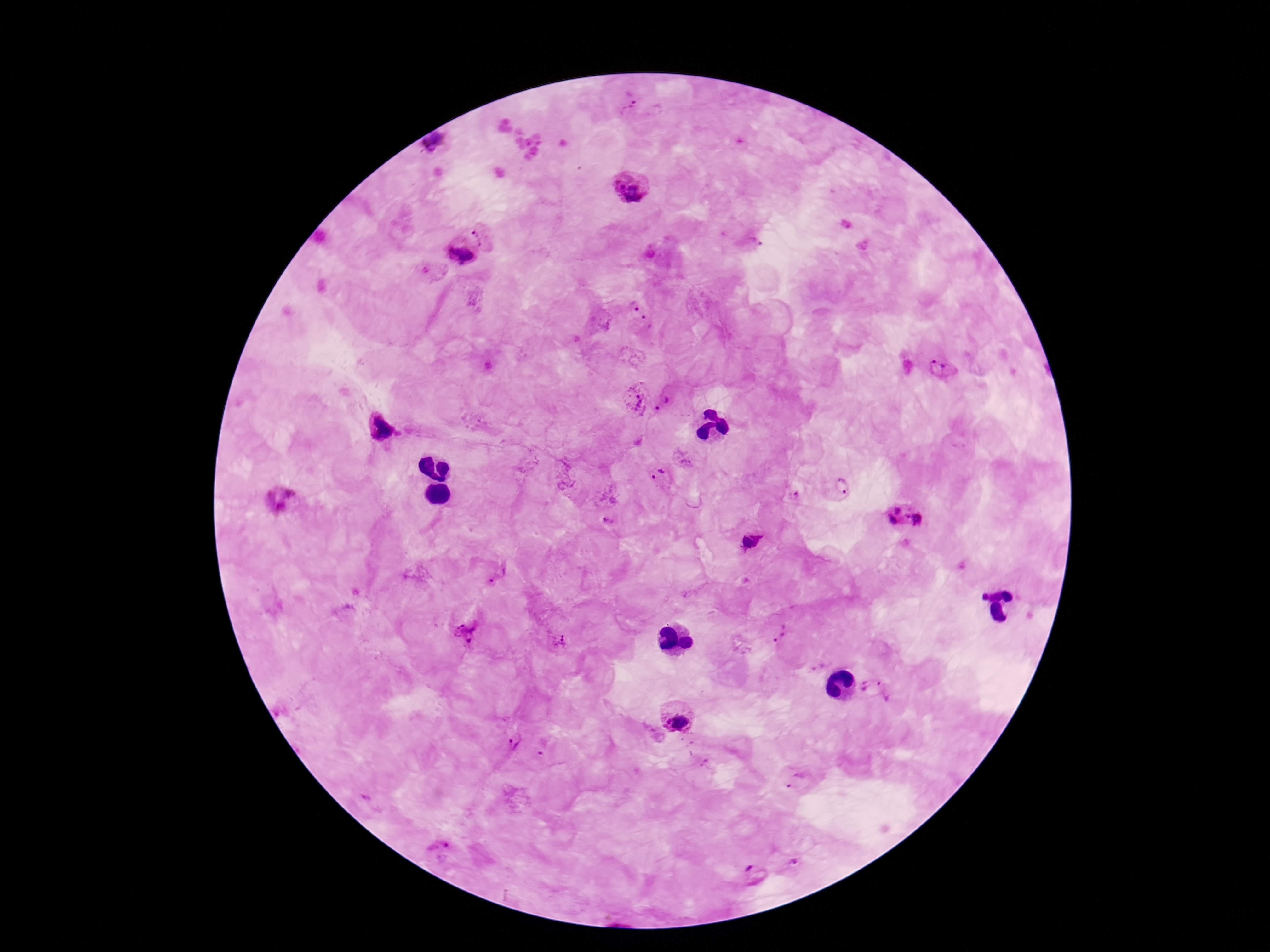
Approximate object centers, in pixels from the top-left corner.
Summary:
  - Plasmodium parasite locations: (x=626, y=106), (x=435, y=145), (x=630, y=185), (x=483, y=236), (x=755, y=241), (x=459, y=253), (x=632, y=305), (x=647, y=323), (x=944, y=369), (x=635, y=398), (x=670, y=406), (x=379, y=427), (x=683, y=460), (x=659, y=475), (x=841, y=484), (x=791, y=495), (x=280, y=500), (x=906, y=517), (x=609, y=519), (x=750, y=542), (x=498, y=573), (x=980, y=596), (x=465, y=632), (x=777, y=633), (x=561, y=640), (x=817, y=667), (x=865, y=685), (x=887, y=689), (x=677, y=716), (x=514, y=739), (x=544, y=746), (x=796, y=782), (x=374, y=800), (x=438, y=851), (x=793, y=861), (x=754, y=872)
  - Capture: smartphone camera through the microscope eyepiece
  - Magnification: 100x
  - Stain: Giemsa
  - Preparation: thick blood smear
  - Patient malaria status: positive
  - Field of view: single
  - Image size: 1270×952 pixels